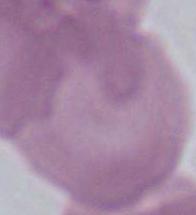
identification = erythrocyte
magnification = 1000x
modality = photomicrograph